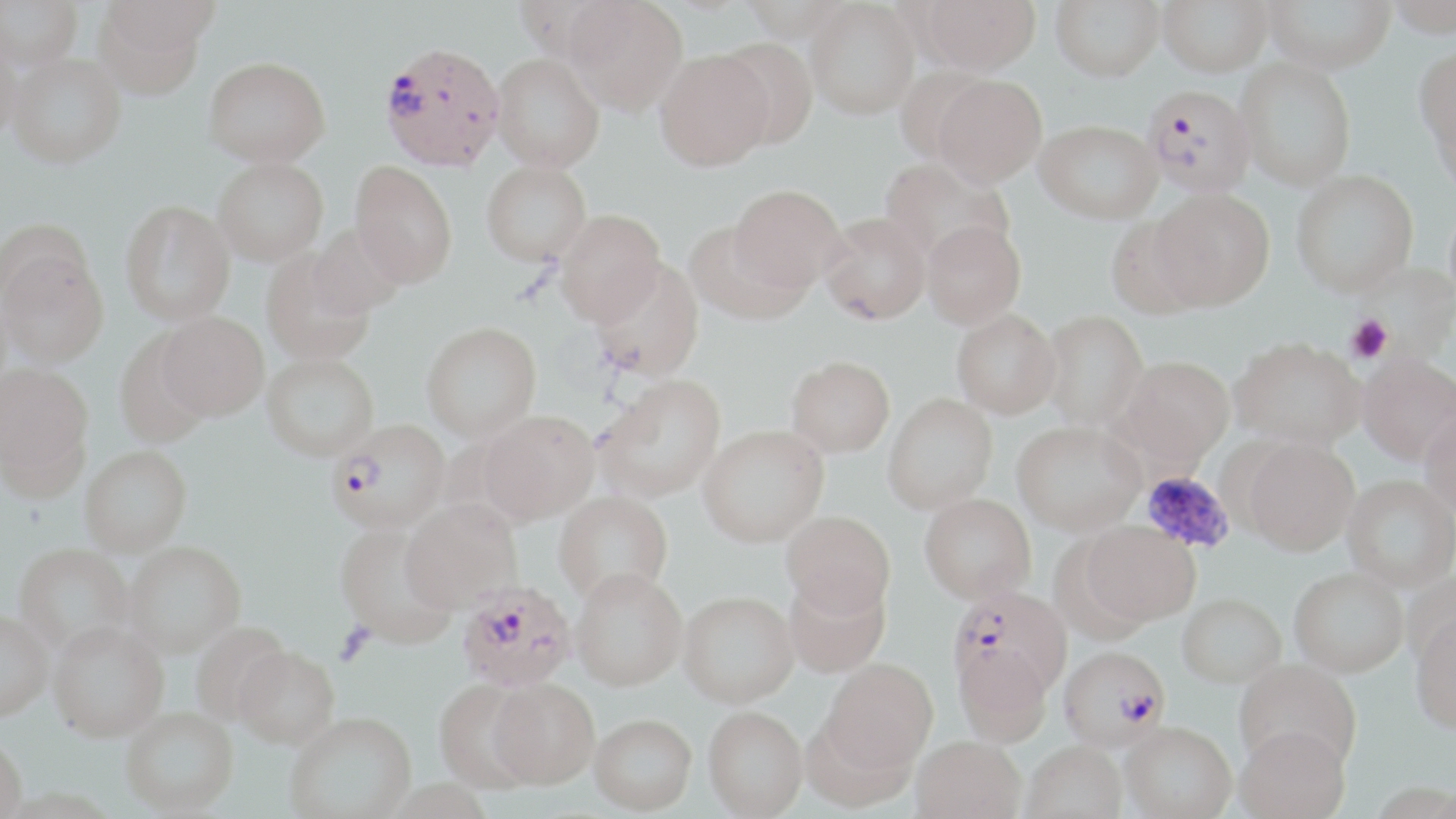
slide-level diagnosis = Plasmodium falciparum
image size = 1456×819 pixels
modality = light microscopy
Plasmodium falciparum-infected red blood cell locations = approximate bounding boxes as (x1, y1, x2, y2) in pixels: (379, 41, 506, 172), (1142, 84, 1256, 196), (328, 421, 452, 539), (457, 586, 575, 695), (948, 591, 1072, 707), (1058, 650, 1169, 757)
preparation = thin blood smear
uninfected red blood cell locations = approximate bounding boxes as (x1, y1, x2, y2) in pixels: (0, 0, 83, 71), (565, 0, 688, 116), (806, 0, 920, 119), (921, 0, 1041, 74), (1051, 0, 1164, 81), (1158, 0, 1273, 76), (1264, 0, 1395, 72), (1386, 0, 1456, 37), (94, 1, 210, 99), (0, 32, 22, 145), (716, 37, 818, 150), (1414, 44, 1456, 158), (654, 50, 774, 171), (7, 52, 125, 168), (491, 53, 605, 172), (203, 57, 331, 167), (1235, 58, 1356, 191), (893, 64, 995, 167), (932, 75, 1047, 188), (1034, 119, 1162, 224), (880, 158, 1013, 267), (213, 160, 329, 270), (481, 162, 592, 271), (348, 165, 457, 290), (1291, 170, 1419, 298), (1151, 188, 1275, 312), (727, 189, 846, 298), (119, 203, 235, 329), (555, 213, 665, 330), (819, 216, 931, 330), (1106, 218, 1206, 321), (922, 222, 1027, 331), (307, 225, 405, 321), (685, 225, 810, 328), (0, 247, 109, 371), (261, 255, 375, 368), (588, 262, 704, 386), (952, 313, 1061, 422), (1042, 314, 1148, 434), (156, 316, 269, 425), (422, 326, 542, 446), (114, 334, 214, 450), (1230, 340, 1366, 454), (1358, 357, 1456, 468), (261, 358, 380, 466), (1117, 359, 1234, 473), (787, 360, 895, 461), (0, 366, 94, 491), (595, 379, 727, 506), (883, 396, 998, 518), (1419, 410, 1456, 522), (479, 414, 600, 528), (1012, 426, 1145, 540), (698, 429, 829, 551), (1242, 442, 1358, 561), (81, 450, 193, 561), (1342, 477, 1455, 595), (554, 495, 673, 611), (919, 498, 1036, 609), (401, 503, 522, 617), (781, 515, 894, 623), (1081, 524, 1199, 630), (334, 528, 457, 651), (124, 545, 246, 663), (13, 546, 134, 661), (1289, 572, 1408, 682), (571, 576, 687, 696), (784, 578, 891, 681), (678, 596, 799, 712), (1177, 597, 1286, 692), (0, 615, 53, 727), (1410, 617, 1456, 739), (190, 623, 293, 729), (47, 627, 169, 746), (952, 646, 1053, 750), (234, 650, 339, 754), (1234, 661, 1361, 779), (821, 662, 939, 779), (488, 682, 599, 794), (434, 683, 540, 795), (703, 710, 808, 819), (120, 711, 239, 818), (801, 716, 914, 816), (286, 717, 417, 819), (590, 719, 697, 818), (1120, 726, 1236, 819), (1235, 730, 1351, 819), (0, 740, 27, 819), (911, 740, 1026, 819), (1021, 745, 1127, 819), (385, 781, 493, 819), (0, 790, 121, 818)
platelet locations = approximate bounding boxes as (x1, y1, x2, y2) in pixels: (1346, 315, 1392, 363), (1139, 470, 1236, 553), (333, 623, 376, 666)
stain = May-Grünwald-Giemsa
magnification = 1000x
field of view = one of a larger specimen